Locate every Plasmodium ovale-infected red blood cell.
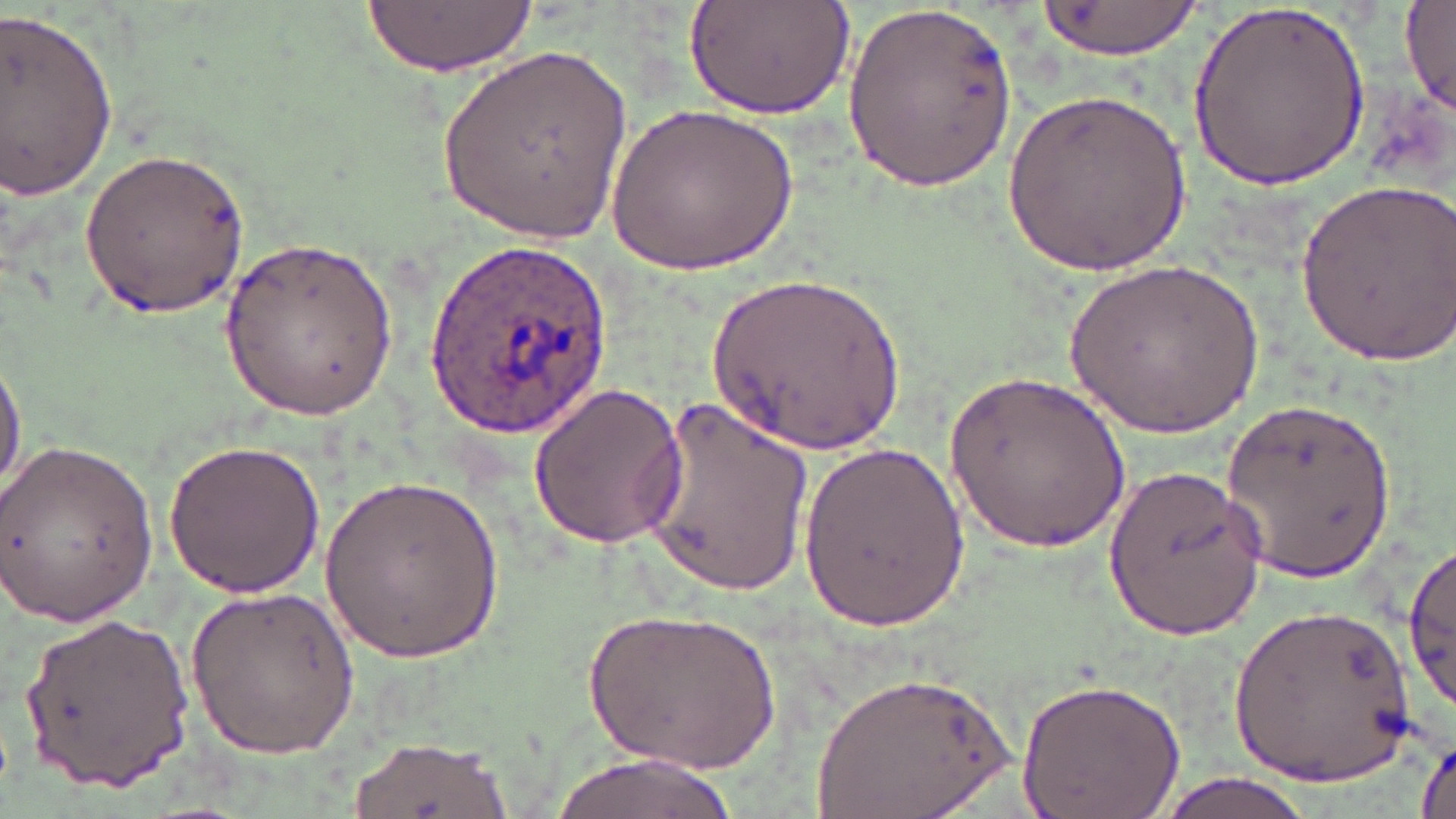
Approximate bounding boxes as [x1, y1, x2, y2] in pixels.
Plasmodium ovale-infected red blood cells: [425, 239, 611, 439].

{
  "slide_level_diagnosis": "Plasmodium ovale",
  "stain": "May-Grünwald-Giemsa",
  "magnification": "1000x",
  "image_size": "1456×819 pixels",
  "modality": "optical microscopy",
  "uninfected_red_blood_cell_locations": "approximate bounding boxes as [x1, y1, x2, y2] in pixels: [361, 0, 533, 79], [684, 0, 857, 118], [842, 0, 1023, 197], [1039, 0, 1205, 60], [1191, 0, 1369, 194], [1402, 3, 1456, 114], [0, 9, 120, 201], [434, 43, 633, 248], [1004, 81, 1191, 278], [611, 99, 797, 273], [79, 144, 251, 315], [1296, 175, 1455, 367], [220, 234, 400, 422], [1065, 255, 1262, 442], [709, 269, 905, 460], [0, 347, 26, 499], [945, 370, 1130, 555], [526, 384, 690, 549], [638, 397, 815, 597], [1219, 400, 1401, 580], [160, 437, 331, 598], [1, 438, 158, 628], [798, 439, 968, 630], [1101, 465, 1273, 639], [321, 471, 503, 667], [1403, 544, 1456, 712], [187, 583, 359, 761], [1232, 601, 1418, 788], [591, 606, 780, 772], [17, 611, 194, 788], [810, 669, 1022, 819], [1016, 676, 1185, 819], [349, 734, 512, 818], [1415, 739, 1455, 819], [550, 753, 740, 819], [1149, 774, 1322, 819]",
  "field_of_view": "single",
  "preparation": "thin blood smear"
}